Name the parasite shown.
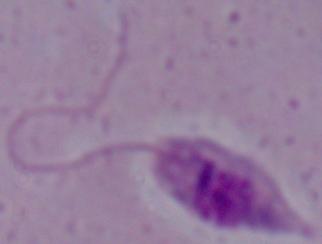
This is Leishmania.

modality = micrograph
magnification = 1000x